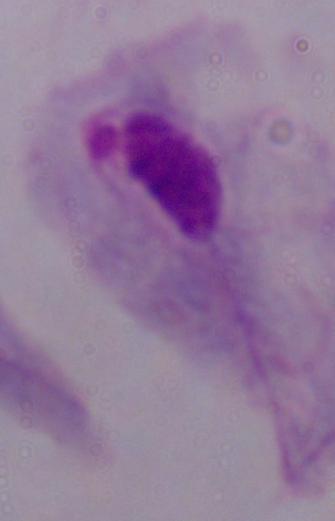

Summary:
  - Magnification: 1000x
  - Identification: trichomonad
  - Modality: micrograph